Look for Plasmodium parasites.
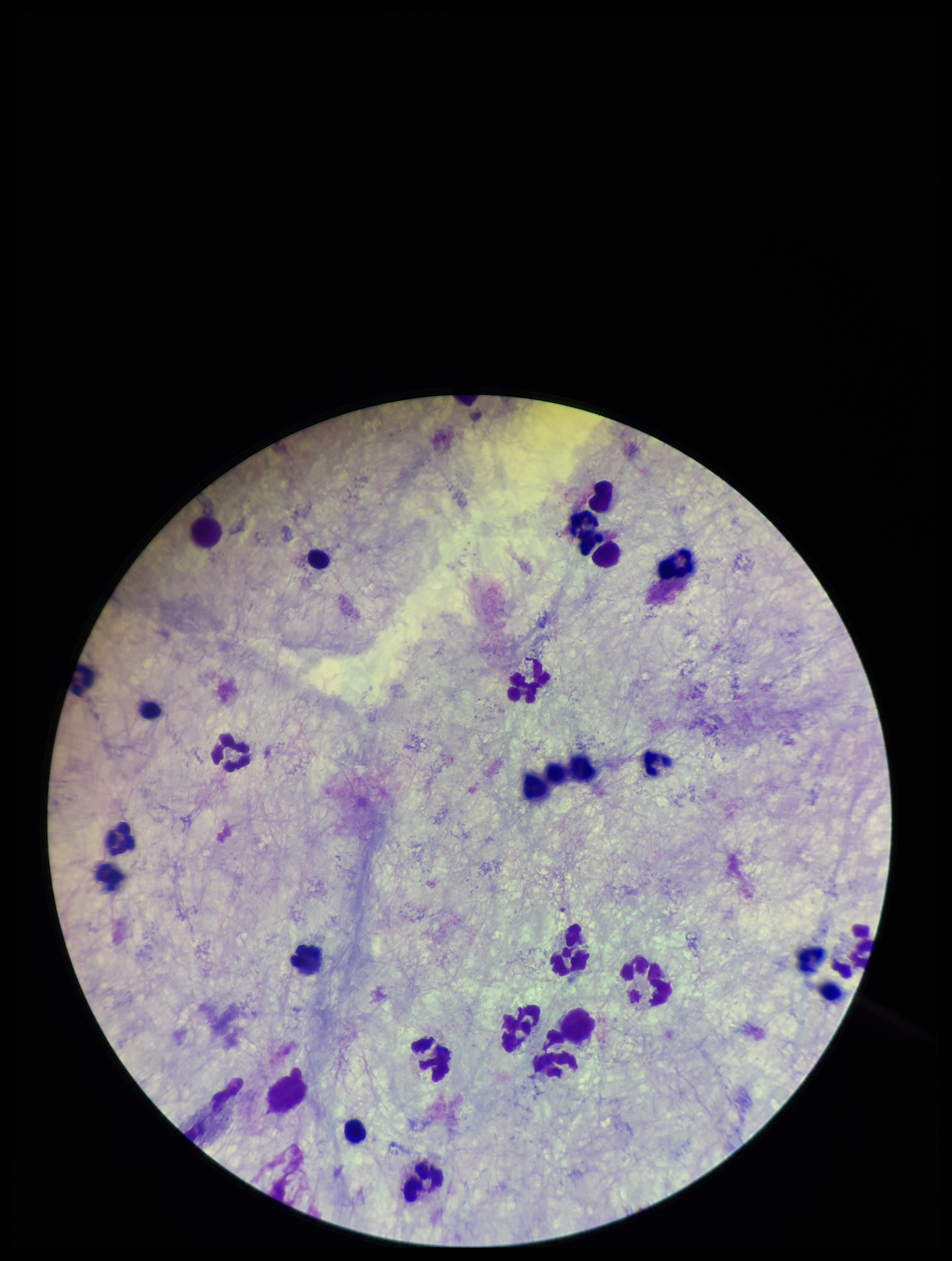

None detected.

Summary:
  - Preparation: thick
  - Patient malaria status: negative
  - Field of view: one from this slide
  - Capture: smartphone photograph through the microscope eyepiece
  - Image size: 952×1261 pixels
  - Leukocyte count: 26
  - Parasite count: 0
  - Stain: Giemsa